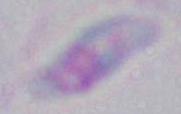

Summary:
  - Identification: Toxoplasma gondii
  - Modality: photomicrograph
  - Magnification: 1000x